Locate every blood parasite and identify its species.
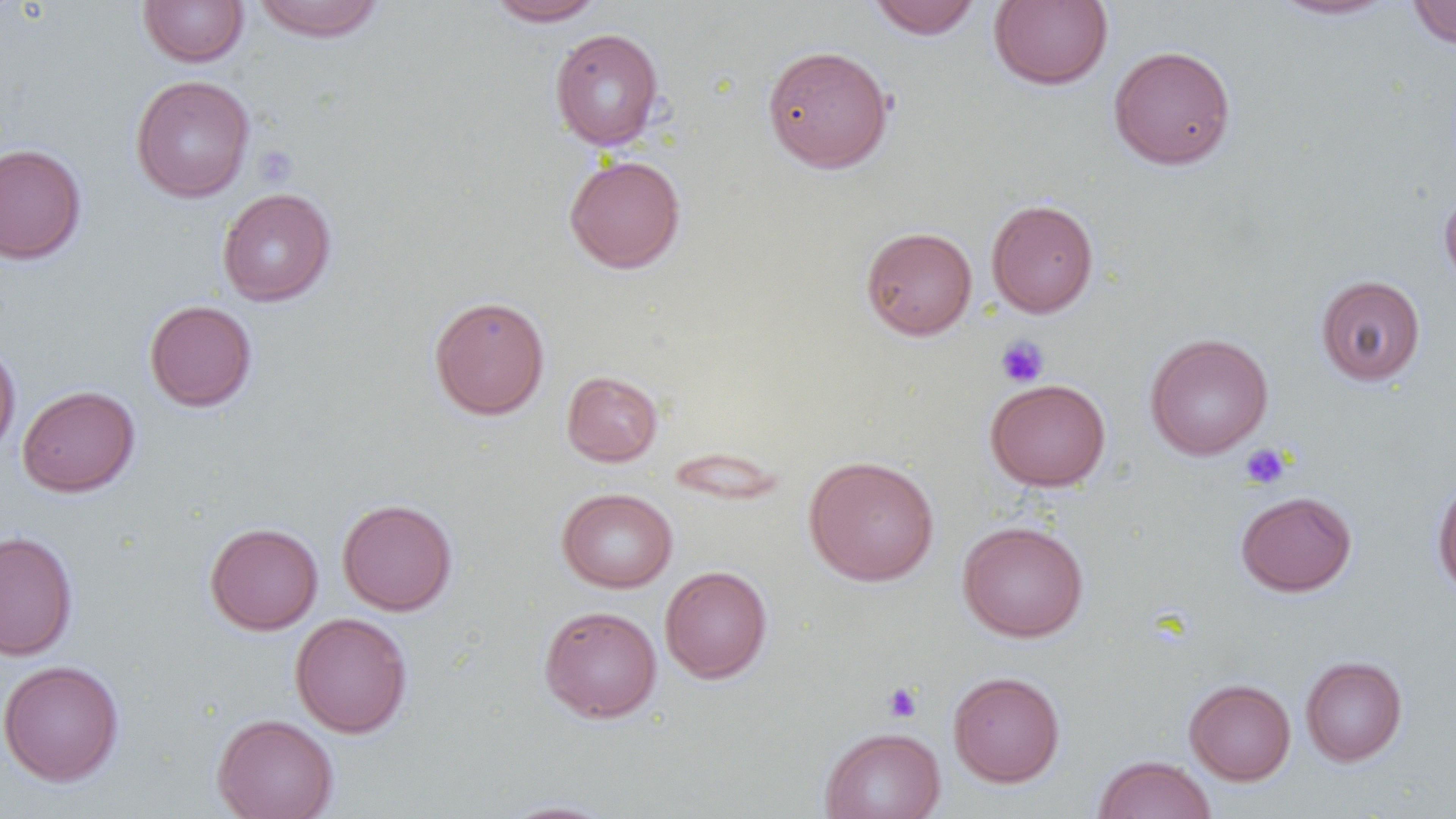
No blood parasites seen.

Approximate bounding boxes as named x1/y1/x2/y2 corners in pixels. Uninfected red blood cell locations: (x1=138, y1=0, x2=249, y2=67), (x1=252, y1=0, x2=385, y2=42), (x1=486, y1=0, x2=606, y2=26), (x1=867, y1=0, x2=982, y2=40), (x1=988, y1=0, x2=1113, y2=90), (x1=1269, y1=0, x2=1399, y2=20), (x1=1407, y1=1, x2=1456, y2=50), (x1=550, y1=28, x2=665, y2=150), (x1=762, y1=44, x2=894, y2=173), (x1=1108, y1=44, x2=1237, y2=170), (x1=130, y1=74, x2=255, y2=202), (x1=0, y1=143, x2=87, y2=265), (x1=564, y1=154, x2=686, y2=274), (x1=217, y1=187, x2=336, y2=306), (x1=1439, y1=188, x2=1456, y2=291), (x1=986, y1=198, x2=1099, y2=318), (x1=860, y1=226, x2=977, y2=340), (x1=1315, y1=275, x2=1426, y2=386), (x1=428, y1=295, x2=550, y2=420), (x1=144, y1=299, x2=258, y2=412), (x1=1145, y1=333, x2=1273, y2=460), (x1=0, y1=342, x2=21, y2=458), (x1=561, y1=370, x2=664, y2=467), (x1=985, y1=378, x2=1111, y2=491), (x1=16, y1=384, x2=140, y2=498), (x1=804, y1=455, x2=940, y2=587), (x1=1432, y1=476, x2=1456, y2=600), (x1=557, y1=487, x2=678, y2=593), (x1=1235, y1=491, x2=1357, y2=596), (x1=337, y1=498, x2=457, y2=616), (x1=958, y1=520, x2=1089, y2=643), (x1=204, y1=522, x2=323, y2=635), (x1=0, y1=530, x2=78, y2=661), (x1=660, y1=565, x2=773, y2=684), (x1=539, y1=605, x2=663, y2=723), (x1=289, y1=612, x2=413, y2=738), (x1=1300, y1=656, x2=1408, y2=766), (x1=0, y1=659, x2=125, y2=786), (x1=947, y1=671, x2=1066, y2=787), (x1=1185, y1=678, x2=1296, y2=785), (x1=212, y1=713, x2=339, y2=819), (x1=820, y1=726, x2=945, y2=819), (x1=1093, y1=755, x2=1216, y2=819), (x1=497, y1=799, x2=623, y2=818). Platelet locations: (x1=253, y1=146, x2=299, y2=188), (x1=996, y1=335, x2=1050, y2=388), (x1=1239, y1=443, x2=1292, y2=490), (x1=882, y1=682, x2=923, y2=723). Slide-level diagnosis: negative for blood parasites. Thin blood film. Image is 1456×819 pixels. One field of a larger specimen. Captured at 1000x magnification. Light microscopy.